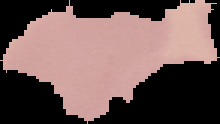

The area outside the segmented cell region is set to black. Image is 220×124 pixels. Malaria status: uninfected. From a thin blood smear.